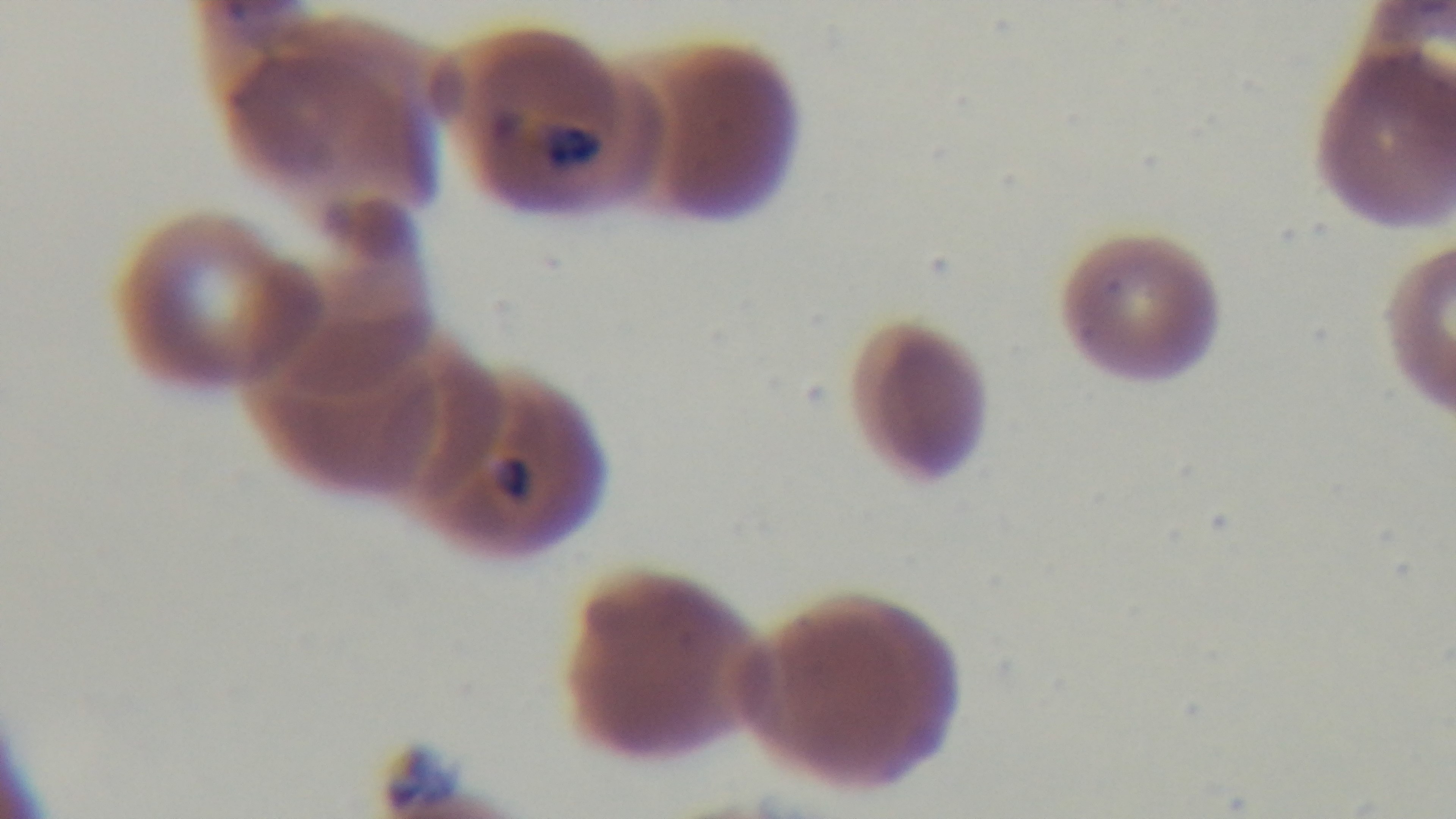
Summary:
  - Capture: mounted 4K digital camera
  - Field of view: single
  - Objective: 100x oil immersion
  - Stain: Giemsa
  - Preparation: thin
  - Modality: light microscopy
  - Malaria status: infected